Comment on the morphology of the erythrocytes.
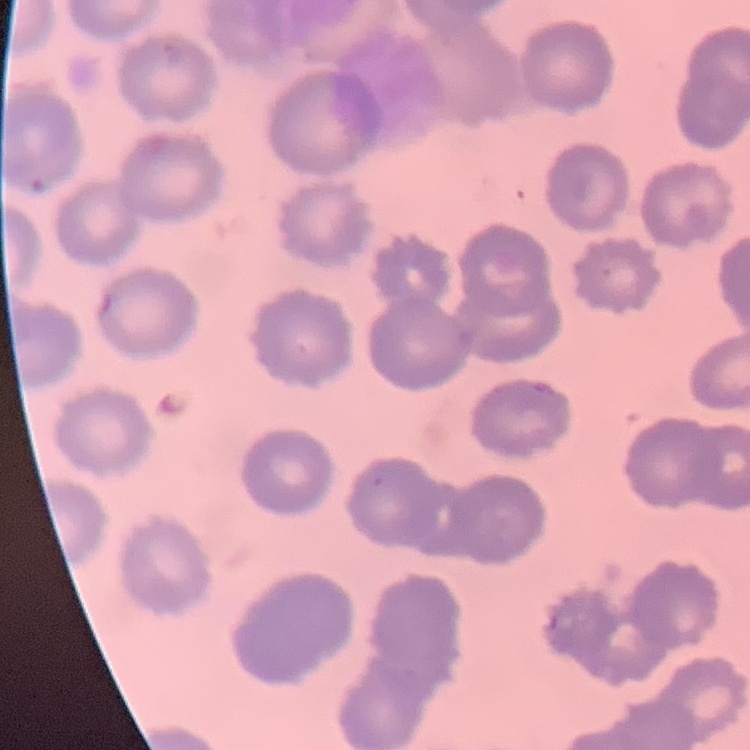

No rouleaux formation.

stain = Field's or Giemsa
preparation = thin peripheral smear
image type = square crop of a larger photomicrograph